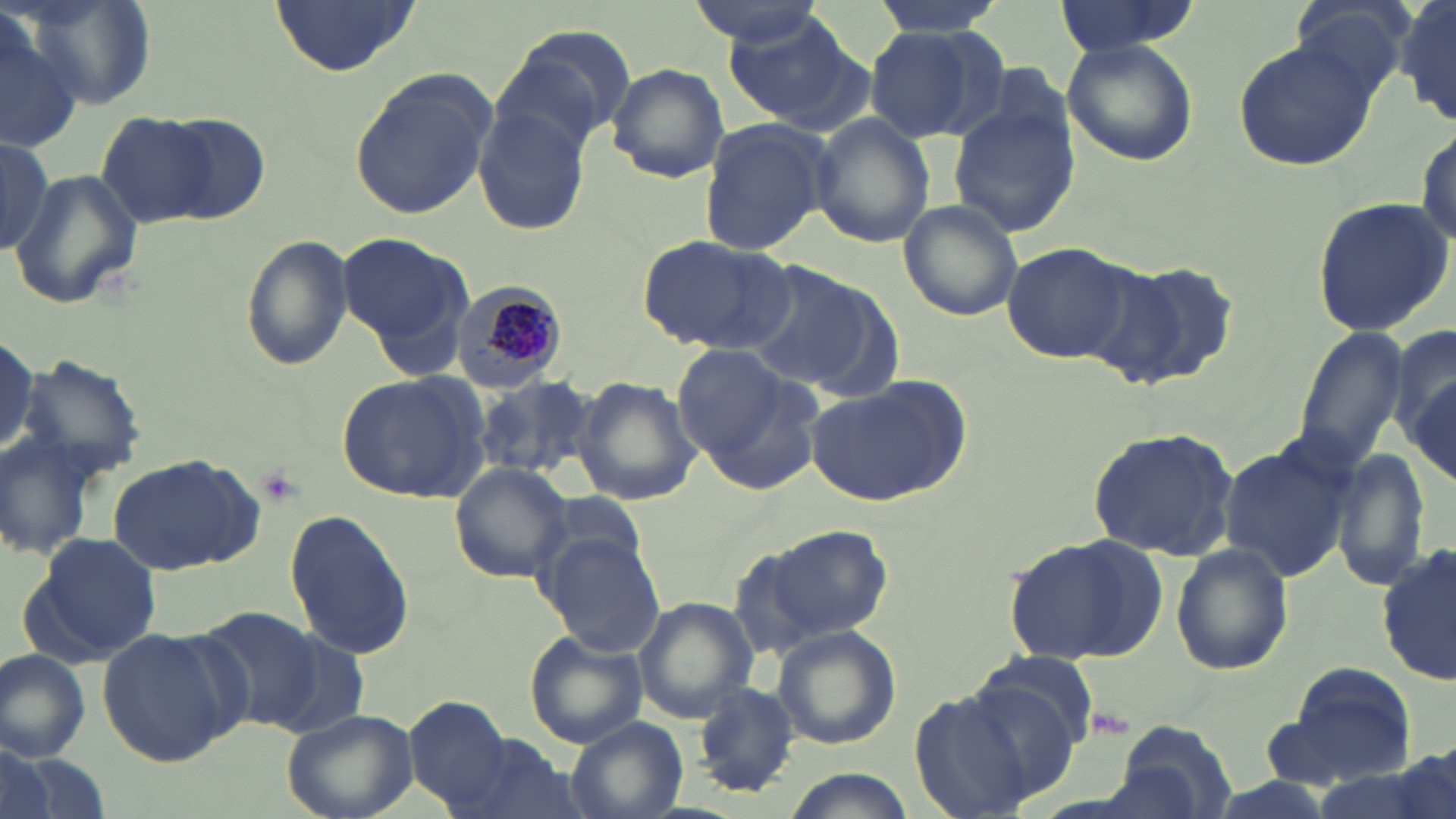

slide-level diagnosis = Plasmodium malariae
field of view = single
image size = 1456×819 pixels
preparation = thin blood film
uninfected red blood cell locations = approximate bounding boxes as (x1, y1, x2, y2) in pixels: (268, 0, 420, 76), (683, 0, 833, 52), (871, 0, 1003, 38), (1050, 0, 1206, 56), (1288, 0, 1418, 108), (1396, 0, 1455, 125), (19, 4, 157, 112), (0, 17, 85, 155), (722, 18, 869, 133), (490, 24, 634, 157), (862, 24, 997, 143), (1062, 39, 1198, 166), (1231, 39, 1380, 173), (605, 61, 730, 183), (348, 68, 496, 223), (947, 100, 1079, 239), (474, 102, 594, 237), (100, 112, 216, 229), (808, 112, 935, 250), (154, 115, 272, 223), (697, 118, 833, 255), (1413, 122, 1454, 252), (1, 137, 55, 256), (9, 168, 143, 309), (1310, 195, 1453, 339), (898, 200, 1024, 322), (339, 231, 471, 358), (239, 234, 354, 370), (636, 234, 797, 355), (1000, 240, 1133, 364), (1097, 259, 1241, 392), (745, 260, 896, 396), (1388, 319, 1456, 459), (1293, 327, 1410, 469), (672, 343, 801, 472), (17, 354, 151, 483), (337, 369, 486, 502), (472, 373, 598, 481), (573, 375, 700, 506), (1407, 375, 1455, 485), (808, 377, 967, 506), (1086, 425, 1240, 560), (1218, 440, 1353, 584), (1332, 449, 1429, 595), (105, 451, 265, 576), (447, 464, 576, 584), (284, 510, 416, 661), (737, 519, 894, 649), (25, 531, 161, 665), (538, 532, 664, 656), (1004, 534, 1171, 666), (1170, 541, 1293, 676), (1378, 542, 1456, 685), (633, 598, 759, 723), (194, 608, 325, 733), (95, 626, 241, 767), (771, 626, 902, 750), (526, 632, 649, 748), (0, 651, 92, 762), (971, 654, 1098, 756), (1270, 665, 1422, 791), (693, 683, 800, 796), (907, 685, 1053, 815), (406, 697, 516, 812), (281, 708, 419, 819), (564, 718, 687, 819), (1109, 720, 1239, 817), (456, 733, 584, 819), (1395, 740, 1454, 819), (0, 746, 84, 819), (785, 770, 916, 819)
Plasmodium malariae-infected red blood cell locations = approximate bounding boxes as (x1, y1, x2, y2) in pixels: (445, 281, 573, 393)
stain = May-Grünwald-Giemsa
modality = light microscopy
magnification = 1000x